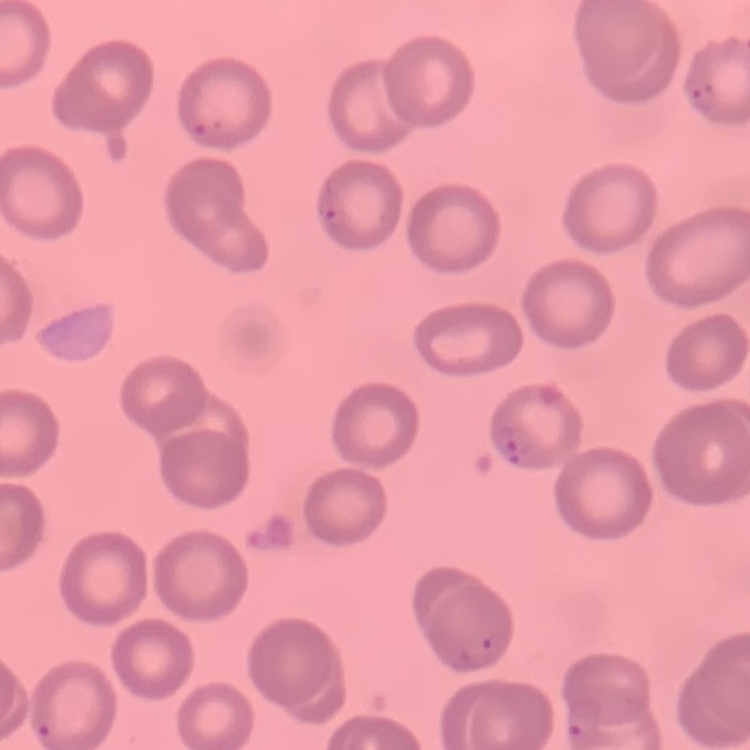
erythrocyte morphology = no rouleaux formation
preparation = thin blood smear
image type = one tile cut from a larger photomicrograph
stain = Field's or Giemsa